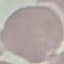
Result: negative for malaria parasites. Photographed with a smartphone camera at the microscope eyepiece. Giemsa-stained preparation. Cell patch, automatically extracted from a larger field of view and resized to 64 × 64 pixels. Thin smear of blood.